Outline each Plasmodium falciparum-infected red blood cell.
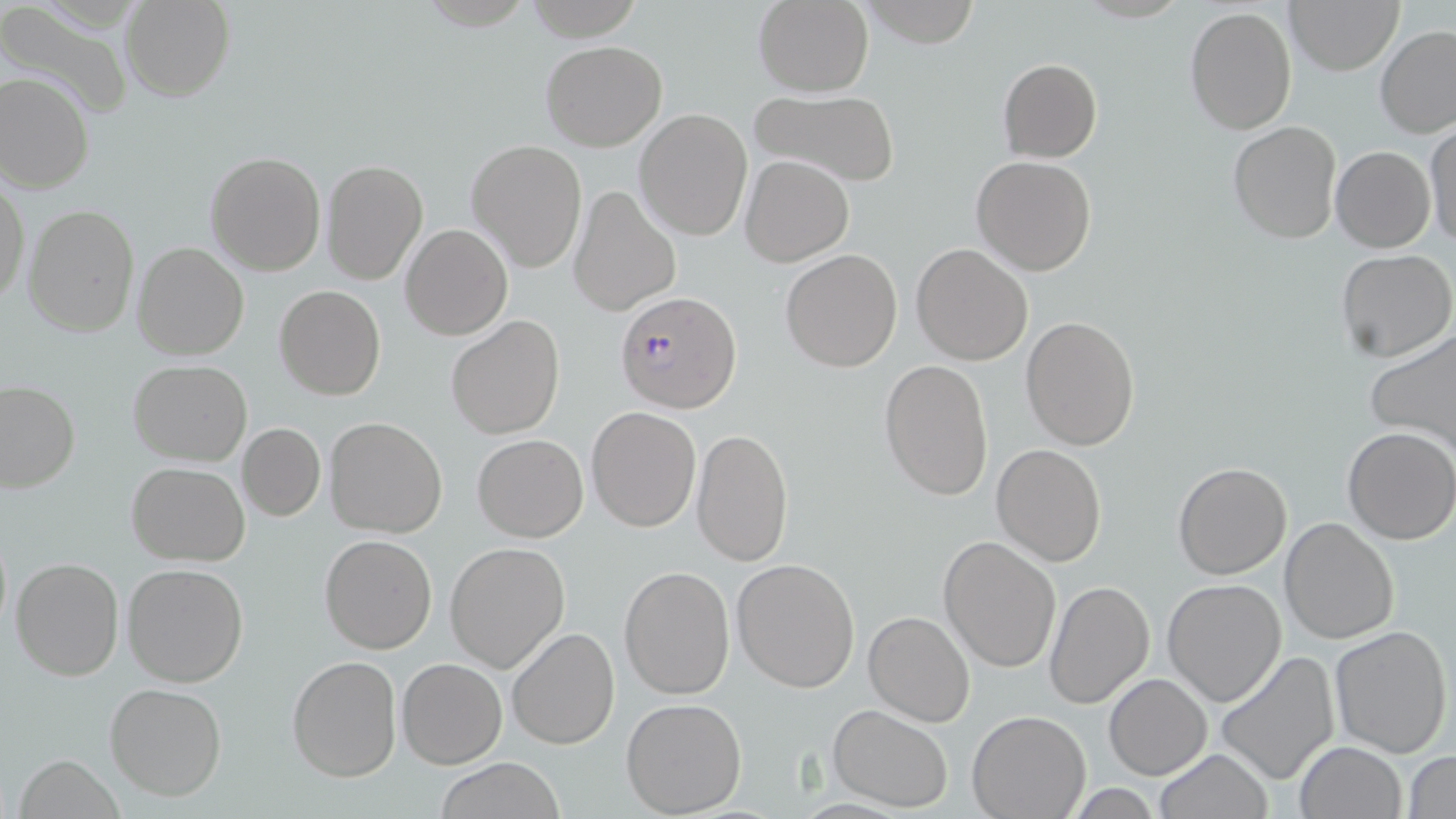
Approximate bounding boxes as named x1/y1/x2/y2 corners in pixels.
Plasmodium falciparum-infected red blood cells: (x1=618, y1=290, x2=740, y2=414).

Uninfected red blood cell locations: (x1=120, y1=0, x2=234, y2=101), (x1=753, y1=0, x2=873, y2=96), (x1=860, y1=0, x2=984, y2=47), (x1=1284, y1=0, x2=1405, y2=74), (x1=0, y1=3, x2=133, y2=120), (x1=1185, y1=5, x2=1297, y2=137), (x1=1375, y1=26, x2=1456, y2=139), (x1=540, y1=40, x2=667, y2=151), (x1=997, y1=58, x2=1101, y2=162), (x1=0, y1=70, x2=94, y2=193), (x1=749, y1=87, x2=899, y2=188), (x1=635, y1=109, x2=753, y2=241), (x1=1227, y1=120, x2=1342, y2=243), (x1=1424, y1=120, x2=1456, y2=248), (x1=466, y1=139, x2=588, y2=272), (x1=1330, y1=145, x2=1436, y2=252), (x1=205, y1=152, x2=326, y2=275), (x1=740, y1=155, x2=853, y2=267), (x1=972, y1=155, x2=1095, y2=277), (x1=322, y1=159, x2=427, y2=285), (x1=1, y1=178, x2=28, y2=307), (x1=568, y1=184, x2=681, y2=316), (x1=24, y1=204, x2=139, y2=336), (x1=400, y1=223, x2=513, y2=342), (x1=133, y1=242, x2=251, y2=363), (x1=912, y1=244, x2=1033, y2=367), (x1=780, y1=249, x2=902, y2=372), (x1=1334, y1=249, x2=1455, y2=364), (x1=275, y1=284, x2=387, y2=401), (x1=446, y1=315, x2=565, y2=440), (x1=1020, y1=317, x2=1140, y2=450), (x1=1365, y1=327, x2=1456, y2=456), (x1=128, y1=360, x2=252, y2=466), (x1=880, y1=360, x2=994, y2=501), (x1=0, y1=382, x2=79, y2=493), (x1=586, y1=407, x2=702, y2=531), (x1=324, y1=417, x2=450, y2=538), (x1=237, y1=422, x2=326, y2=521), (x1=1342, y1=426, x2=1456, y2=545), (x1=691, y1=428, x2=794, y2=566), (x1=471, y1=434, x2=588, y2=542), (x1=992, y1=444, x2=1107, y2=566), (x1=1173, y1=462, x2=1291, y2=580), (x1=127, y1=463, x2=251, y2=564), (x1=1280, y1=517, x2=1399, y2=644), (x1=320, y1=534, x2=436, y2=654), (x1=938, y1=535, x2=1062, y2=672), (x1=444, y1=542, x2=570, y2=672), (x1=10, y1=557, x2=125, y2=681), (x1=731, y1=557, x2=860, y2=692), (x1=122, y1=562, x2=249, y2=687), (x1=619, y1=565, x2=735, y2=698), (x1=1044, y1=579, x2=1155, y2=709), (x1=1161, y1=579, x2=1287, y2=706), (x1=864, y1=610, x2=976, y2=728), (x1=1329, y1=625, x2=1452, y2=757), (x1=506, y1=627, x2=620, y2=750), (x1=1214, y1=649, x2=1341, y2=786), (x1=287, y1=655, x2=402, y2=783), (x1=396, y1=658, x2=506, y2=769), (x1=1104, y1=674, x2=1211, y2=780), (x1=105, y1=682, x2=227, y2=800), (x1=621, y1=698, x2=747, y2=817), (x1=828, y1=704, x2=955, y2=814), (x1=967, y1=708, x2=1090, y2=818), (x1=1294, y1=740, x2=1407, y2=819), (x1=1155, y1=748, x2=1272, y2=819), (x1=1405, y1=751, x2=1456, y2=818), (x1=14, y1=754, x2=124, y2=819), (x1=433, y1=758, x2=568, y2=818). Slide-level diagnosis: Plasmodium falciparum. Captured at 1000x magnification. Thin blood film. May-Grünwald-Giemsa stain. Light microscopy. Image is 1456×819 pixels. Single field of view.